Outline each blood parasite and name the species.
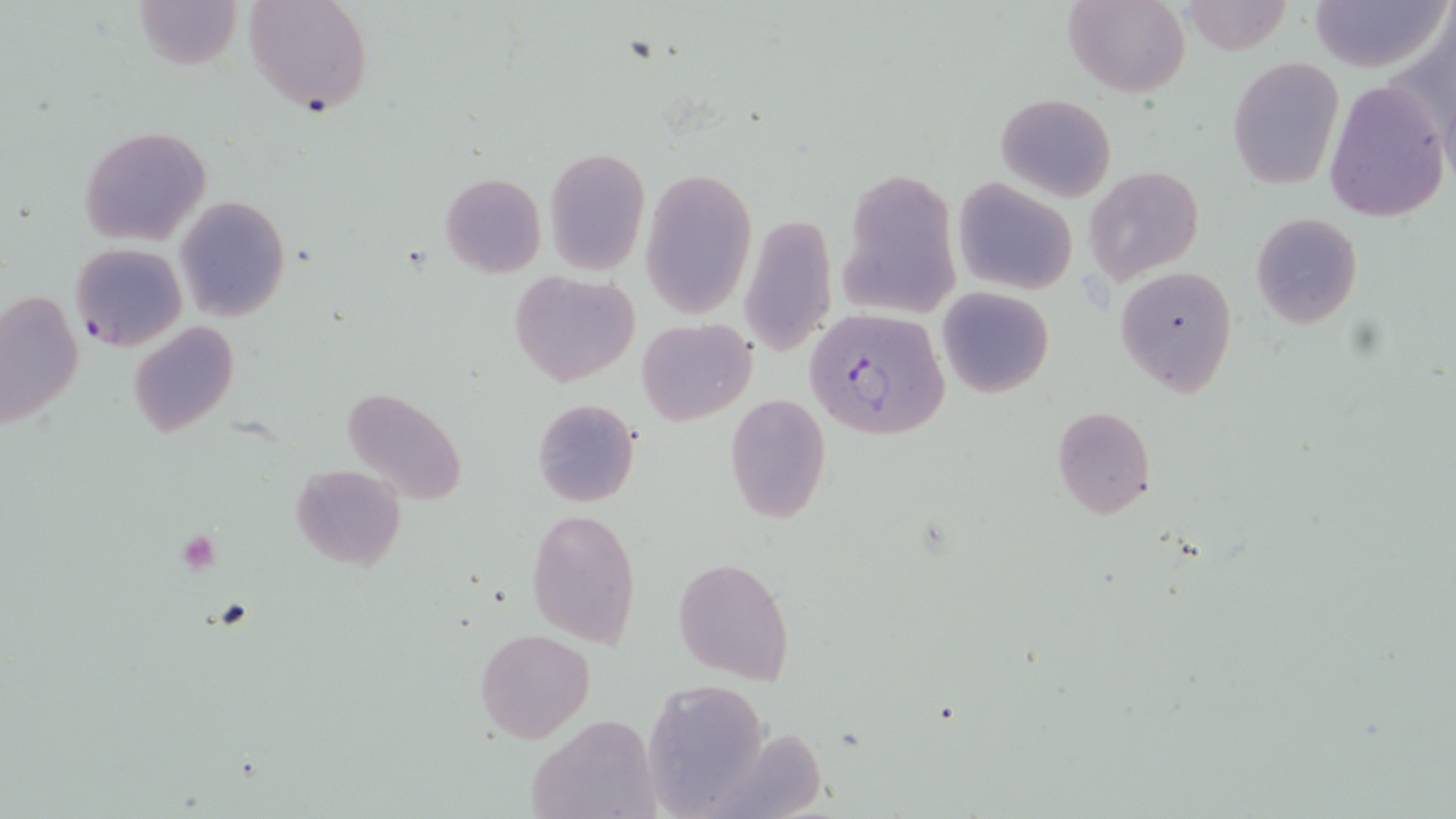

Approximate bounding boxes as named x1/y1/x2/y2 corners in pixels.
Plasmodium falciparum-infected red blood cells: (x1=71, y1=242, x2=187, y2=350), (x1=809, y1=308, x2=951, y2=441).
No Plasmodium ovale, Plasmodium malariae, Plasmodium vivax, Babesia divergens, or Trypanosoma brucei observed.

Summary:
  - Platelet locations: (x1=179, y1=531, x2=219, y2=575)
  - Uninfected red blood cell locations: (x1=133, y1=0, x2=244, y2=71), (x1=244, y1=0, x2=373, y2=117), (x1=1064, y1=0, x2=1190, y2=98), (x1=1307, y1=0, x2=1448, y2=74), (x1=1180, y1=1, x2=1291, y2=54), (x1=1227, y1=56, x2=1344, y2=190), (x1=1324, y1=77, x2=1450, y2=222), (x1=996, y1=93, x2=1115, y2=202), (x1=78, y1=126, x2=212, y2=246), (x1=543, y1=146, x2=650, y2=275), (x1=640, y1=166, x2=759, y2=318), (x1=1084, y1=167, x2=1204, y2=284), (x1=836, y1=168, x2=959, y2=318), (x1=440, y1=172, x2=546, y2=277), (x1=952, y1=179, x2=1079, y2=294), (x1=175, y1=196, x2=290, y2=321), (x1=739, y1=212, x2=837, y2=359), (x1=1250, y1=213, x2=1362, y2=328), (x1=1115, y1=265, x2=1237, y2=395), (x1=507, y1=271, x2=642, y2=385), (x1=937, y1=287, x2=1054, y2=399), (x1=0, y1=290, x2=85, y2=430), (x1=637, y1=318, x2=758, y2=425), (x1=130, y1=322, x2=239, y2=439), (x1=341, y1=385, x2=469, y2=507), (x1=723, y1=393, x2=833, y2=523), (x1=532, y1=398, x2=640, y2=508), (x1=1051, y1=406, x2=1156, y2=520), (x1=290, y1=464, x2=405, y2=569), (x1=526, y1=507, x2=643, y2=647), (x1=673, y1=556, x2=795, y2=684), (x1=476, y1=628, x2=596, y2=742), (x1=641, y1=682, x2=772, y2=815), (x1=526, y1=713, x2=660, y2=819)
  - Slide-level diagnosis: Plasmodium falciparum
  - Stain: May-Grünwald-Giemsa
  - Field of view: single
  - Image size: 1456×819 pixels
  - Magnification: 1000x
  - Preparation: thin blood smear
  - Modality: optical microscopy